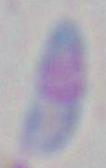

modality: micrograph
identification: Toxoplasma gondii
magnification: 1000x